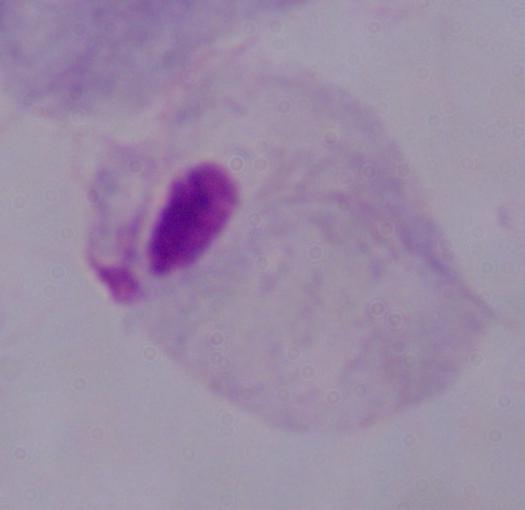

Summary:
  - Modality: photomicrograph
  - Identification: trichomonad
  - Magnification: 1000x